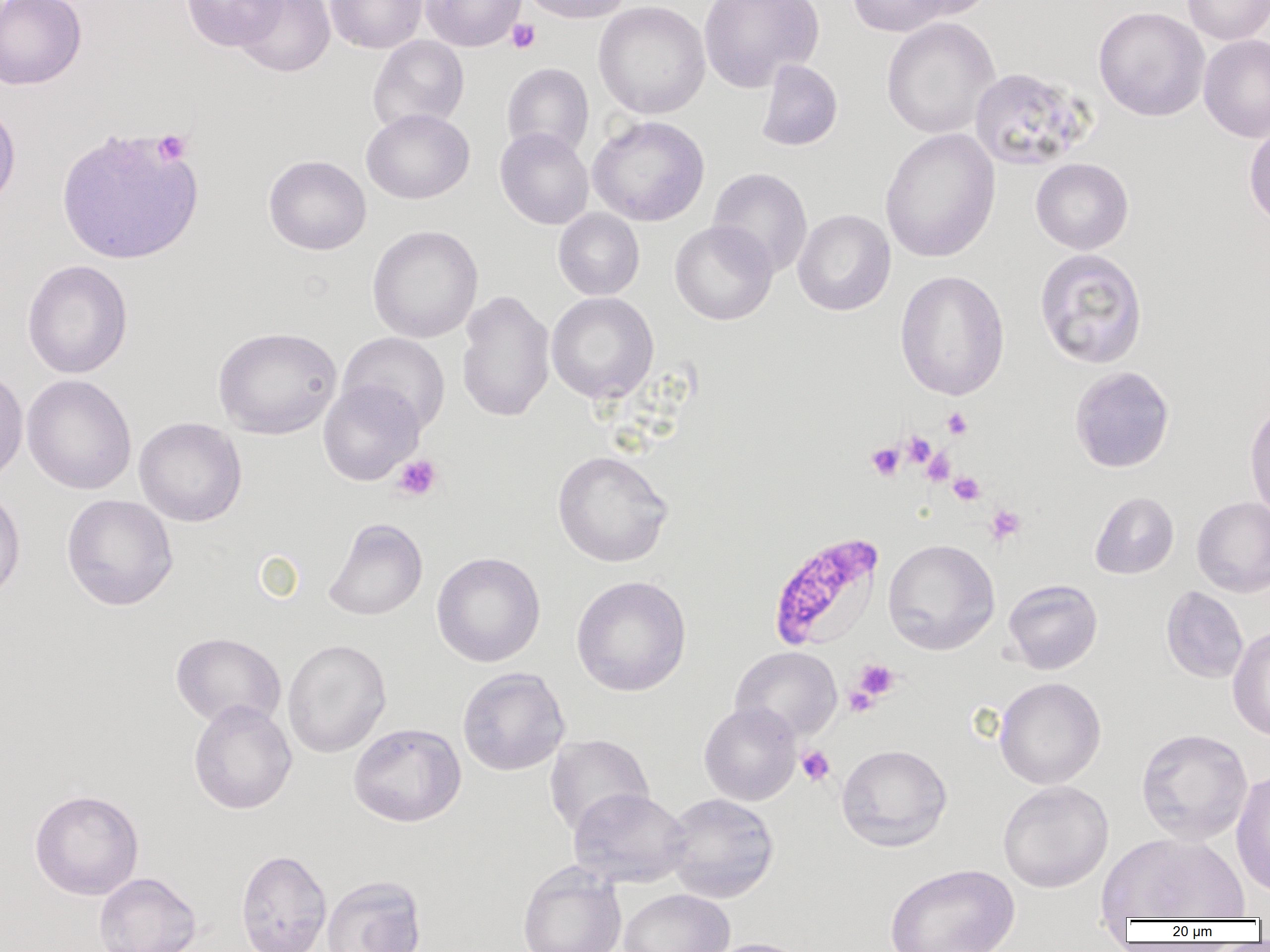
slide-level diagnosis = Plasmodium falciparum
platelet locations = approximate bounding boxes as (x1, y1, x2, y2) in pixels: (506, 19, 541, 54), (152, 129, 192, 165), (942, 408, 973, 439), (901, 432, 937, 468), (866, 443, 905, 480), (922, 449, 955, 485), (392, 454, 443, 501), (948, 471, 985, 506), (984, 504, 1026, 545), (852, 659, 900, 701), (843, 684, 879, 718), (796, 745, 835, 786)
magnification = 1000x
Plasmodium falciparum-infected red blood cell locations = approximate bounding boxes as (x1, y1, x2, y2) in pixels: (767, 531, 886, 653)
image size = 1270×952 pixels
field of view = single
preparation = thin blood film
modality = optical microscopy
uninfected red blood cell locations = approximate bounding boxes as (x1, y1, x2, y2) in pixels: (0, 0, 86, 90), (180, 0, 286, 51), (232, 0, 335, 77), (325, 0, 428, 53), (420, 0, 527, 51), (519, 0, 633, 24), (698, 0, 824, 92), (847, 0, 952, 36), (901, 0, 998, 21), (1181, 0, 1270, 45), (593, 1, 711, 119), (1093, 6, 1210, 121), (881, 17, 1001, 139), (1198, 34, 1270, 143), (368, 35, 469, 133), (755, 59, 843, 152), (501, 63, 594, 160), (969, 66, 1094, 171), (0, 101, 21, 211), (361, 108, 475, 204), (587, 115, 710, 227), (1243, 120, 1270, 228), (56, 126, 204, 266), (495, 127, 594, 230), (880, 127, 1001, 264), (263, 155, 371, 255), (1030, 158, 1134, 254), (708, 167, 812, 278), (553, 208, 644, 300), (792, 209, 896, 316), (669, 220, 777, 325), (367, 225, 483, 343), (1034, 248, 1148, 369), (22, 260, 133, 379), (895, 270, 1010, 401), (456, 289, 555, 423), (546, 292, 659, 404), (213, 326, 342, 439), (337, 332, 451, 435), (0, 365, 28, 488), (1069, 366, 1175, 473), (21, 374, 137, 495), (318, 379, 424, 485), (1244, 400, 1270, 520), (134, 417, 247, 527), (552, 450, 673, 567), (0, 485, 26, 603), (1089, 491, 1179, 579), (61, 494, 178, 611), (1192, 496, 1270, 597), (323, 517, 427, 621), (882, 538, 1000, 655), (431, 551, 545, 667), (571, 575, 691, 697), (1002, 579, 1103, 674), (1161, 585, 1248, 684), (1227, 625, 1270, 742), (170, 632, 286, 729), (282, 638, 391, 758), (731, 646, 843, 742), (457, 667, 570, 776), (994, 676, 1106, 789), (188, 700, 297, 815), (699, 701, 802, 806), (348, 723, 466, 827), (1135, 728, 1253, 845), (544, 734, 654, 837), (836, 743, 952, 852), (1231, 769, 1270, 897), (997, 780, 1114, 893), (569, 788, 692, 889), (29, 789, 144, 900), (661, 792, 780, 903), (1098, 831, 1250, 921), (235, 849, 332, 952), (517, 862, 627, 952), (884, 862, 1020, 952), (93, 872, 201, 952), (321, 875, 427, 952), (618, 888, 734, 952), (702, 937, 814, 952)